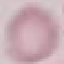

Summary:
  - Result: no malaria parasites detected
  - Stain: Giemsa
  - Image type: automatically extracted cell patch, resized to 64 × 64 pixels
  - Preparation: thin blood film
  - Capture: smartphone camera at the microscope eyepiece